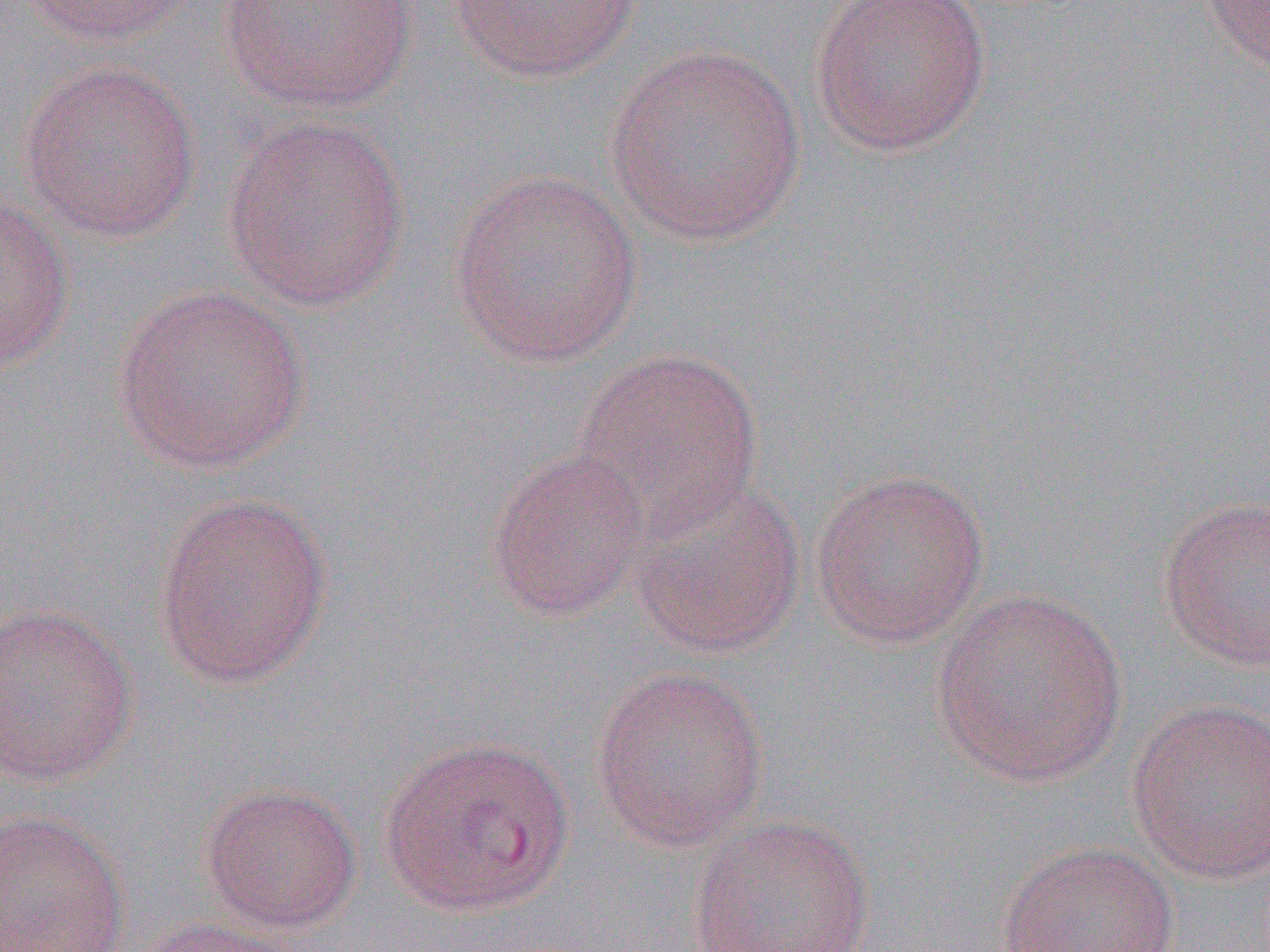

Approximate bounding boxes as [x1, y1, x2, y2] in pixels. Uninfected red blood cell locations: [16, 0, 202, 48], [217, 0, 421, 114], [446, 0, 644, 83], [809, 0, 993, 157], [1197, 0, 1270, 76], [604, 42, 807, 246], [19, 60, 201, 242], [221, 115, 411, 312], [448, 167, 644, 369], [0, 193, 74, 374], [111, 283, 309, 474], [573, 349, 763, 529], [483, 447, 652, 622], [808, 466, 990, 649], [627, 475, 806, 659], [150, 490, 335, 690], [1157, 495, 1270, 672], [930, 589, 1128, 789], [0, 600, 140, 789], [590, 665, 769, 851], [1126, 696, 1270, 885], [377, 734, 574, 917], [198, 782, 363, 934], [0, 809, 132, 952], [685, 814, 877, 952], [996, 841, 1180, 952], [127, 916, 306, 952]. Slide-level diagnosis: Plasmodium vivax. Image is 1270×952 pixels. Light microscopy. 1000x magnification. One field of a larger specimen. Thin blood film.